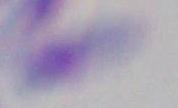
{
  "magnification": "1000x",
  "identification": "Toxoplasma gondii",
  "modality": "photomicrograph"
}